Point out each Plasmodium parasite.
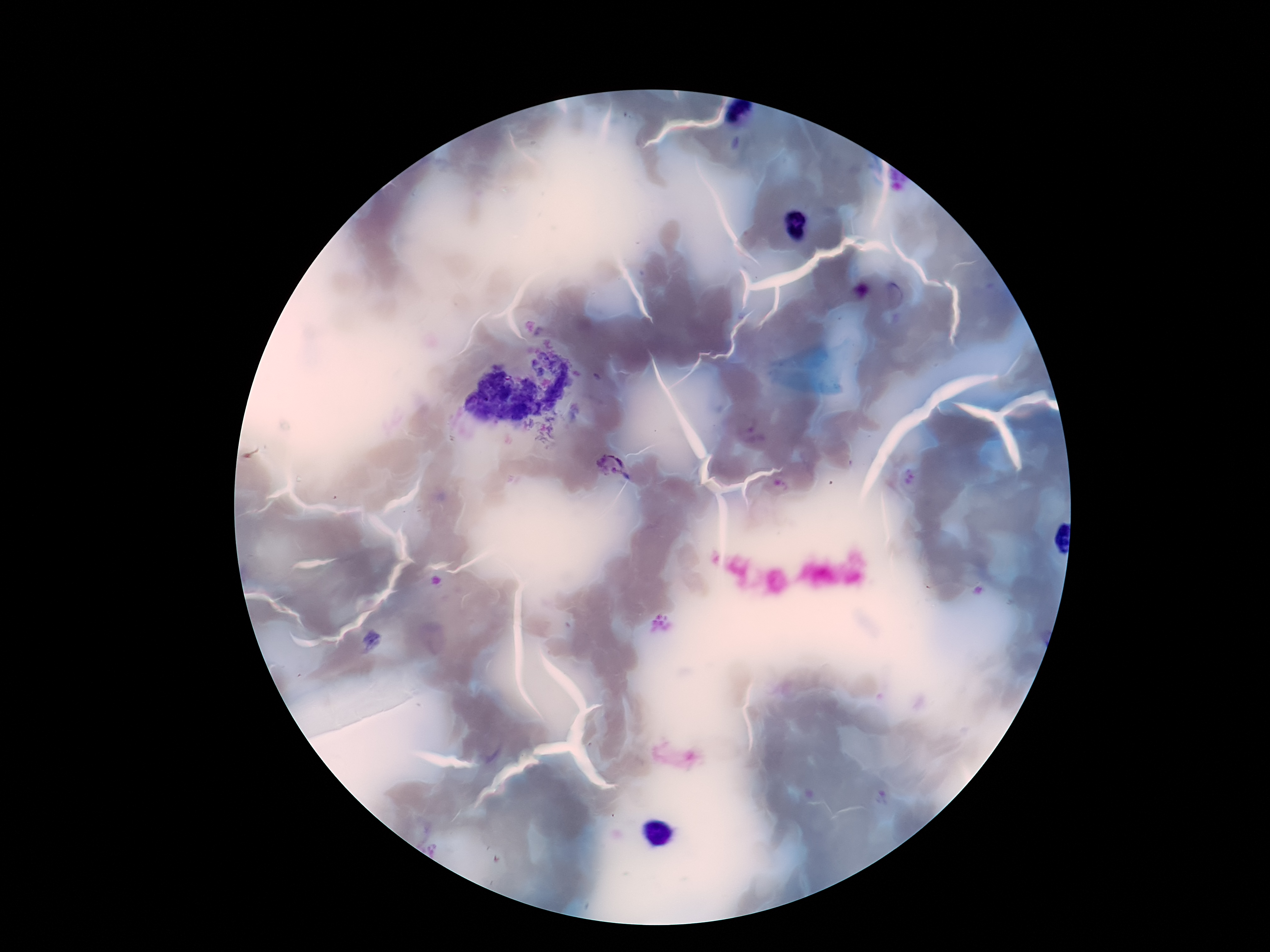
Approximate centers as [x, y] in pixels.
Plasmodium parasites: [896, 296], [612, 467].

Summary:
  - Stain: Giemsa
  - Preparation: thick peripheral-blood smear
  - Field of view: one from this slide
  - Magnification: 100x
  - Capture: smartphone camera through the microscope eyepiece
  - Patient malaria status: positive
  - Image size: 1270×952 pixels